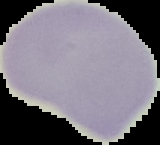

From a thin blood film. Segmented cell region on a black background. Image is 160×145 pixels. Malaria status: uninfected.